Name the blood parasite species.
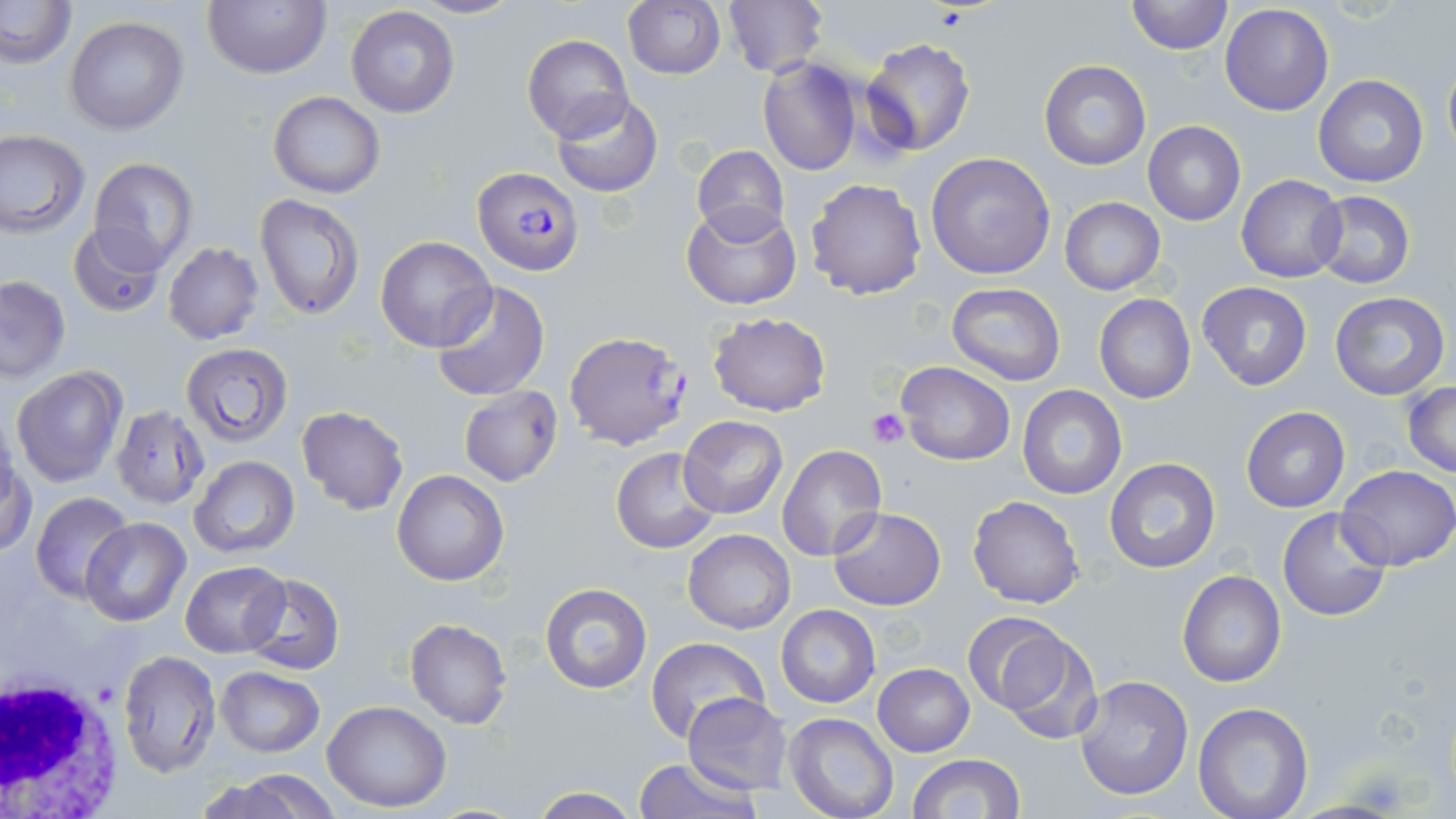
Plasmodium falciparum.

{
  "white_blood_cell_locations": "approximate bounding boxes as named x1/y1/x2/y2 corners in pixels: (x1=0, y1=670, x2=129, y2=814)",
  "plasmodium_falciparum_infected_red_blood_cell_locations": "approximate bounding boxes as named x1/y1/x2/y2 corners in pixels: (x1=473, y1=167, x2=584, y2=275)",
  "magnification": "1000x",
  "platelet_locations": "approximate bounding boxes as named x1/y1/x2/y2 corners in pixels: (x1=867, y1=408, x2=911, y2=448)",
  "modality": "optical microscopy",
  "uninfected_red_blood_cell_locations": "approximate bounding boxes as named x1/y1/x2/y2 corners in pixels: (x1=0, y1=0, x2=76, y2=68), (x1=202, y1=0, x2=330, y2=79), (x1=406, y1=0, x2=524, y2=20), (x1=622, y1=0, x2=725, y2=80), (x1=1125, y1=0, x2=1230, y2=56), (x1=721, y1=1, x2=827, y2=77), (x1=1220, y1=4, x2=1334, y2=115), (x1=345, y1=5, x2=460, y2=118), (x1=65, y1=17, x2=189, y2=135), (x1=522, y1=34, x2=633, y2=143), (x1=860, y1=37, x2=976, y2=156), (x1=1442, y1=50, x2=1456, y2=165), (x1=758, y1=58, x2=861, y2=175), (x1=1039, y1=60, x2=1151, y2=170), (x1=1314, y1=74, x2=1428, y2=188), (x1=268, y1=92, x2=384, y2=198), (x1=551, y1=94, x2=664, y2=198), (x1=1143, y1=120, x2=1247, y2=226), (x1=0, y1=129, x2=90, y2=236), (x1=692, y1=144, x2=789, y2=242), (x1=925, y1=152, x2=1057, y2=281), (x1=89, y1=157, x2=200, y2=271), (x1=1237, y1=174, x2=1346, y2=282), (x1=805, y1=177, x2=928, y2=301), (x1=1309, y1=191, x2=1416, y2=290), (x1=254, y1=192, x2=366, y2=320), (x1=1059, y1=197, x2=1166, y2=295), (x1=682, y1=203, x2=800, y2=311), (x1=67, y1=223, x2=168, y2=316), (x1=374, y1=237, x2=496, y2=353), (x1=163, y1=243, x2=264, y2=346), (x1=0, y1=275, x2=70, y2=381), (x1=429, y1=281, x2=551, y2=404), (x1=1196, y1=281, x2=1313, y2=389), (x1=944, y1=284, x2=1066, y2=386), (x1=1329, y1=290, x2=1451, y2=402), (x1=1093, y1=294, x2=1196, y2=405), (x1=706, y1=311, x2=832, y2=417), (x1=563, y1=330, x2=692, y2=451), (x1=183, y1=343, x2=292, y2=448), (x1=897, y1=361, x2=1014, y2=465), (x1=11, y1=365, x2=126, y2=485), (x1=1402, y1=382, x2=1456, y2=477), (x1=1016, y1=385, x2=1126, y2=499), (x1=459, y1=386, x2=563, y2=485), (x1=297, y1=405, x2=409, y2=515), (x1=113, y1=406, x2=213, y2=506), (x1=1241, y1=406, x2=1350, y2=512), (x1=679, y1=416, x2=788, y2=520), (x1=777, y1=445, x2=888, y2=564), (x1=611, y1=446, x2=721, y2=554), (x1=3, y1=456, x2=37, y2=559), (x1=189, y1=456, x2=300, y2=558), (x1=1105, y1=457, x2=1221, y2=573), (x1=1339, y1=465, x2=1456, y2=571), (x1=393, y1=470, x2=509, y2=585), (x1=29, y1=491, x2=134, y2=600), (x1=967, y1=494, x2=1086, y2=609), (x1=828, y1=507, x2=946, y2=610), (x1=1277, y1=507, x2=1390, y2=623), (x1=81, y1=517, x2=190, y2=626), (x1=683, y1=529, x2=795, y2=633), (x1=181, y1=560, x2=291, y2=658), (x1=1176, y1=570, x2=1287, y2=688), (x1=241, y1=573, x2=344, y2=676), (x1=540, y1=583, x2=652, y2=693), (x1=774, y1=604, x2=882, y2=708), (x1=961, y1=612, x2=1070, y2=715), (x1=404, y1=618, x2=512, y2=729), (x1=988, y1=625, x2=1104, y2=744), (x1=646, y1=638, x2=769, y2=745), (x1=117, y1=650, x2=219, y2=777), (x1=873, y1=663, x2=975, y2=756), (x1=215, y1=666, x2=324, y2=758), (x1=1073, y1=675, x2=1195, y2=802), (x1=682, y1=693, x2=793, y2=794), (x1=322, y1=700, x2=452, y2=812), (x1=1192, y1=702, x2=1314, y2=819), (x1=784, y1=713, x2=899, y2=819), (x1=907, y1=753, x2=1025, y2=819), (x1=631, y1=758, x2=761, y2=819), (x1=202, y1=771, x2=339, y2=819), (x1=530, y1=787, x2=641, y2=819)",
  "field_of_view": "single",
  "stain": "May-Grünwald-Giemsa",
  "preparation": "thin blood film",
  "image_size": "1456×819 pixels"
}